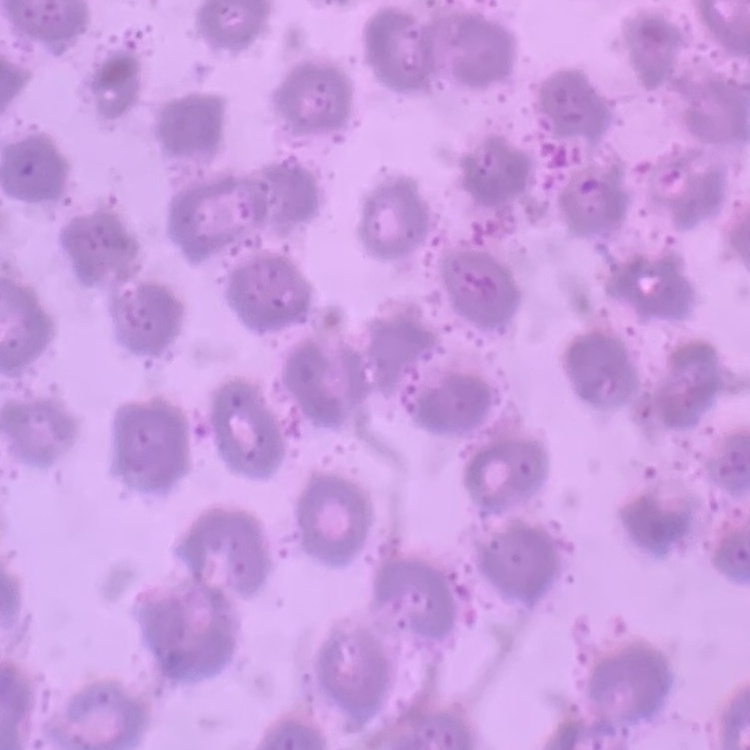
Summary:
  - Erythrocyte morphology: no rouleaux formation
  - Preparation: thin peripheral smear
  - Stain: Field's or Giemsa
  - Image type: one tile cut from a larger photomicrograph